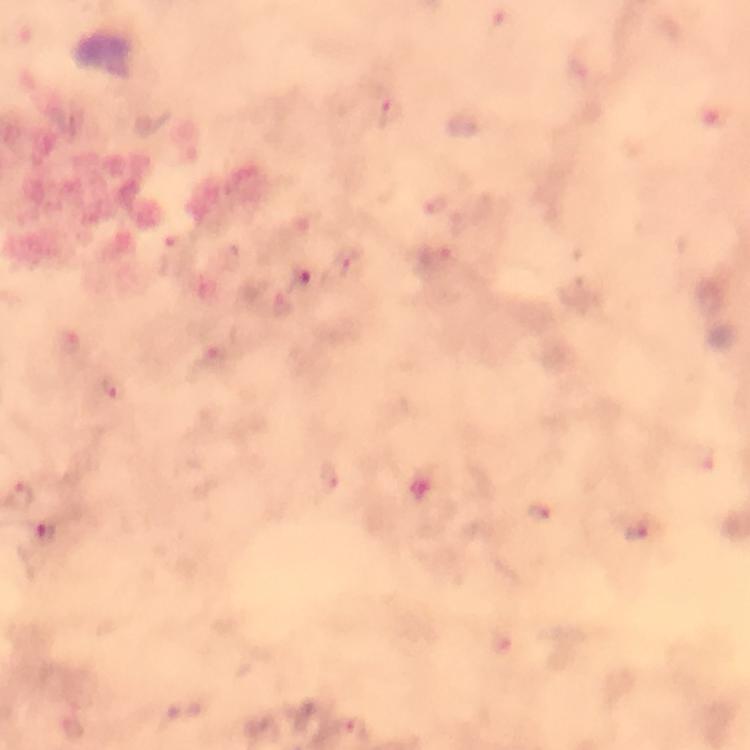
cropped from = one field of view
preparation = thick smear
capture = smartphone mounted on the microscope
image size = 750×750 pixels
immersion oil = applied
stain = Giemsa
malaria parasite locations = approximate centers as (x, y) in pixels: (391, 112), (302, 280), (215, 358), (114, 390), (328, 480), (20, 496), (540, 511), (636, 535), (350, 731)
magnification = 100x
context = from a malaria diagnostic workup